Identify the parasite.
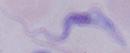
A trypanosome.

Micrograph. Captured at 1000x magnification.